State the blood parasite species.
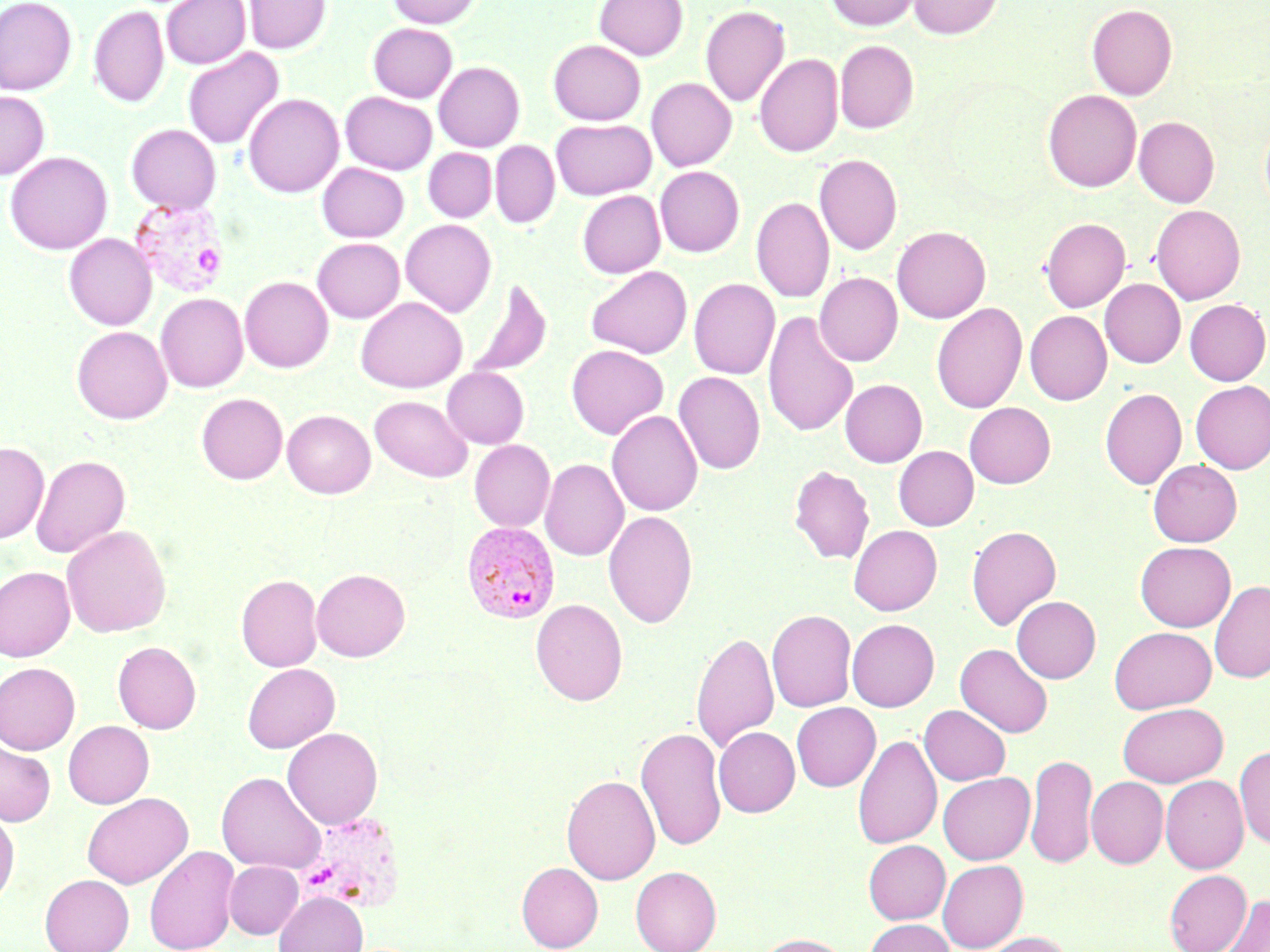
Plasmodium vivax.

Summary:
  - Coordinate format: approximate bounding boxes as [x1, y1, x2, y2] in pixels
  - Plasmodium vivax-infected red blood cell locations: [128, 195, 231, 298], [462, 522, 560, 624]
  - Uninfected red blood cell locations: [0, 0, 77, 95], [161, 0, 250, 69], [244, 0, 331, 55], [388, 0, 482, 28], [594, 0, 688, 60], [825, 0, 921, 30], [908, 0, 1004, 39], [1086, 3, 1177, 100], [700, 5, 790, 108], [88, 6, 169, 108], [368, 23, 458, 102], [548, 39, 646, 125], [835, 39, 919, 133], [183, 48, 284, 150], [754, 52, 843, 157], [434, 61, 525, 151], [646, 78, 736, 171], [1042, 89, 1142, 192], [0, 91, 50, 179], [340, 91, 437, 174], [243, 93, 344, 198], [1134, 116, 1219, 207], [550, 118, 656, 200], [1260, 119, 1270, 216], [126, 124, 221, 214], [490, 140, 559, 229], [423, 147, 496, 223], [5, 151, 112, 255], [814, 154, 902, 256], [316, 162, 409, 242], [655, 166, 744, 256], [577, 191, 665, 278], [751, 196, 835, 304], [1150, 205, 1245, 304], [1040, 217, 1130, 311], [400, 219, 496, 317], [892, 226, 991, 323], [64, 233, 157, 330], [312, 237, 404, 323], [586, 265, 692, 358], [814, 273, 903, 366], [239, 276, 333, 373], [466, 277, 553, 379], [688, 278, 780, 379], [1100, 279, 1185, 368], [155, 293, 248, 392], [355, 296, 467, 393], [1184, 299, 1270, 385], [931, 303, 1027, 414], [762, 310, 859, 439], [1024, 310, 1112, 405], [72, 326, 172, 424], [566, 344, 668, 440], [442, 367, 529, 448], [673, 371, 765, 475], [840, 379, 927, 467], [1190, 381, 1270, 473], [1100, 388, 1187, 490], [196, 393, 287, 484], [369, 395, 473, 483], [964, 402, 1055, 488], [282, 409, 375, 498], [607, 410, 703, 516], [469, 439, 555, 531], [0, 441, 49, 544], [893, 445, 978, 531], [31, 454, 130, 558], [540, 458, 628, 561], [1148, 459, 1242, 546], [789, 465, 875, 564], [603, 510, 698, 628], [61, 524, 171, 638], [848, 525, 942, 615], [966, 525, 1061, 631], [1135, 541, 1235, 631], [0, 566, 75, 662], [311, 568, 410, 661], [236, 574, 323, 672], [1210, 580, 1270, 684], [1012, 595, 1101, 683], [530, 599, 628, 705], [767, 609, 856, 712], [847, 619, 939, 711], [1109, 626, 1216, 713], [691, 630, 779, 754], [112, 641, 201, 734], [955, 643, 1053, 738], [0, 663, 81, 754], [242, 663, 340, 753], [791, 702, 881, 791], [1118, 703, 1227, 786], [919, 705, 1010, 785], [63, 721, 154, 809], [635, 726, 726, 852], [282, 727, 383, 829], [714, 727, 799, 817], [852, 733, 942, 850], [0, 740, 55, 826], [1234, 745, 1270, 849], [1026, 753, 1097, 869], [216, 771, 326, 874], [938, 772, 1035, 864], [561, 774, 660, 884], [1161, 775, 1248, 873], [1086, 777, 1168, 868], [82, 793, 192, 889], [0, 810, 20, 908], [863, 840, 950, 924], [144, 846, 238, 952], [937, 860, 1028, 951], [224, 861, 303, 939], [516, 861, 603, 951], [630, 866, 721, 952], [1164, 869, 1251, 951], [40, 874, 134, 952], [273, 891, 368, 952], [1220, 894, 1270, 951], [864, 919, 955, 952], [976, 931, 1073, 952], [754, 933, 850, 952]
  - Magnification: 1000x
  - Image size: 1270×952 pixels
  - Stain: May-Grünwald-Giemsa
  - Preparation: thin blood smear
  - Field of view: one of a larger specimen
  - Modality: optical microscopy